Comment on the morphology of the red blood cells.
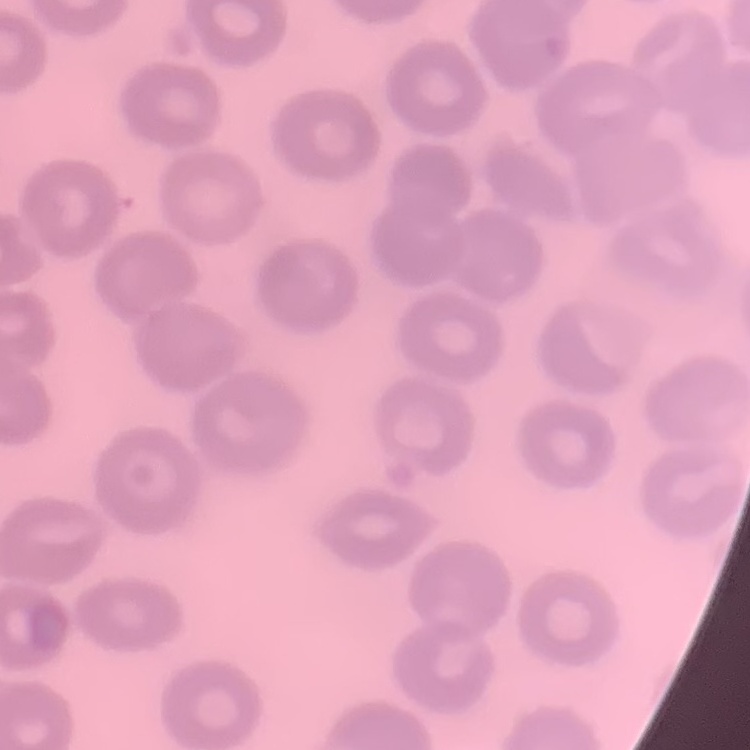
No rouleaux formation.

Summary:
  - Image type: square crop of a larger photomicrograph
  - Stain: Field's or Giemsa
  - Preparation: thin blood smear